Assess this cell for malaria.
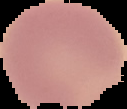
Uninfected.

Cell region segmented out of the field of view; the surrounding area is masked to black. Image is 127×109 pixels. From a thin blood film.